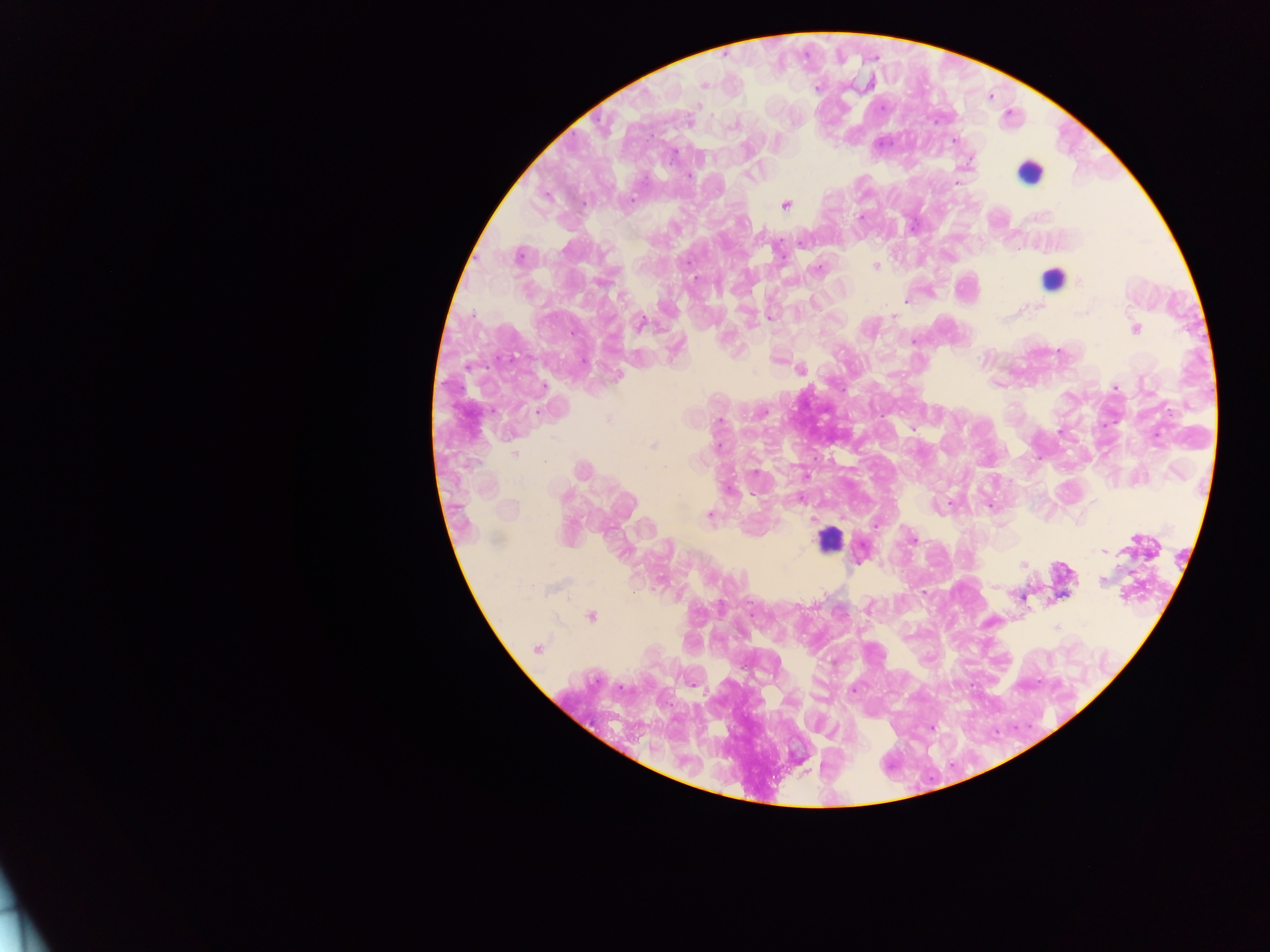
Approximate centers as x y in pixels. Malaria parasite locations: 702 85; 697 106; 688 122; 733 123; 954 140; 688 176; 957 184; 785 205; 860 217; 518 256; 875 266; 816 267; 620 296; 908 300; 1038 306; 893 316; 640 322; 1134 329; 675 348; 1060 351; 776 358; 800 369; 617 375; 1115 387; 717 421; 1058 432; 653 446; 582 470; 754 472; 801 498; 950 503; 988 505; 709 514; 876 524; 911 539; 1103 550; 1022 564; 1100 580; 1021 597; 868 607; 591 616; 536 648; 853 690; 932 727. Leukocyte locations: 1028 171; 1052 280; 829 539; 1059 582. Sample from Ghana. Thick blood smear. One field of view. Photographed through a microscope with a mobile-phone camera. Image is 1270×952 pixels.